Locate every malaria parasite and every leukocyte.
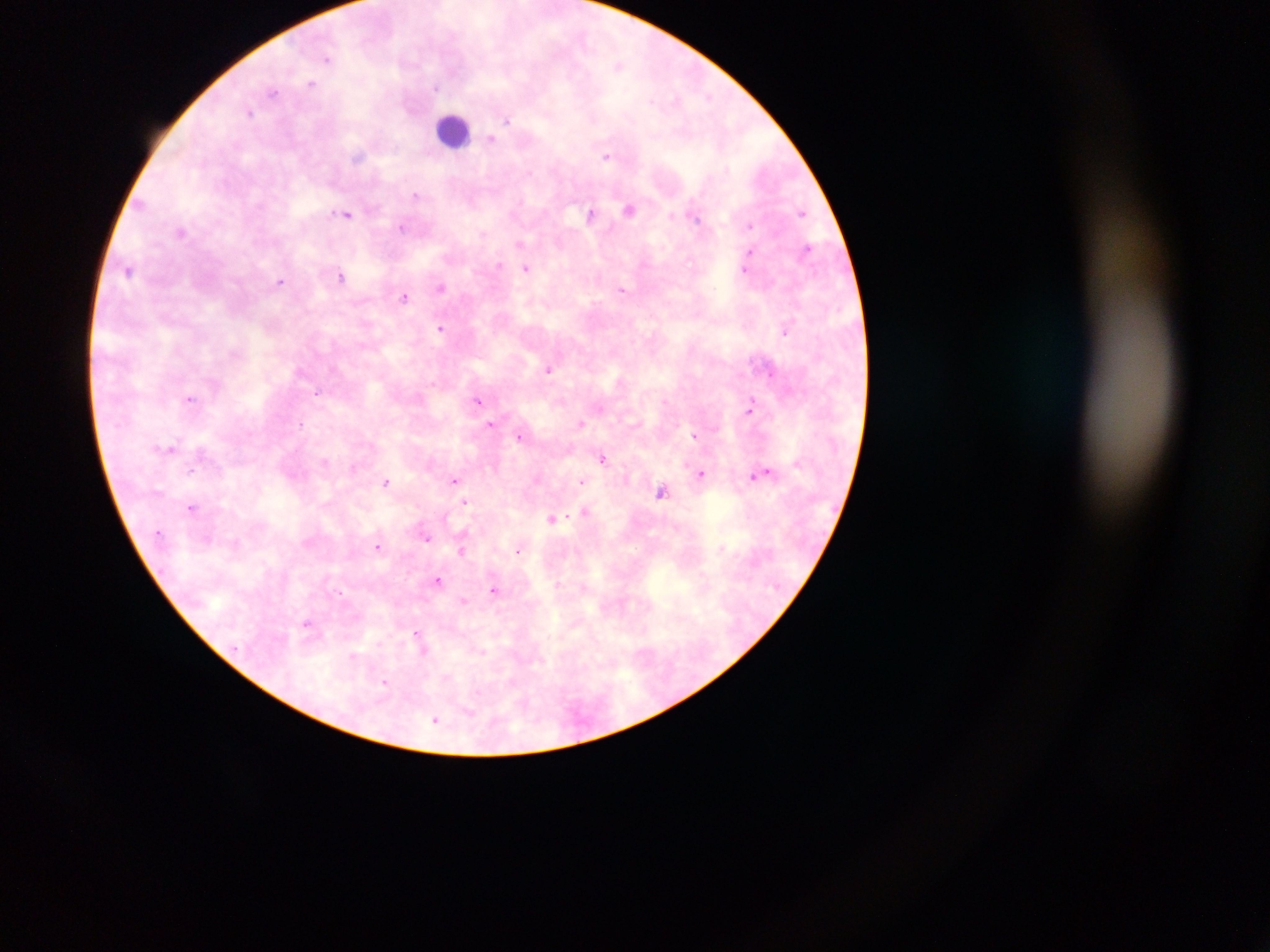

Approximate centers as {x, y} in pixels.
Malaria parasites: {327, 58}, {619, 66}, {311, 84}, {436, 87}, {273, 92}, {651, 100}, {250, 112}, {507, 120}, {491, 139}, {606, 155}, {358, 157}, {530, 173}, {415, 194}, {142, 204}, {629, 209}, {802, 212}, {347, 214}, {590, 214}, {672, 216}, {696, 217}, {748, 225}, {402, 227}, {182, 232}, {807, 249}, {750, 252}, {499, 266}, {526, 267}, {745, 269}, {129, 271}, {341, 276}, {280, 282}, {441, 288}, {621, 289}, {404, 298}, {440, 327}, {785, 331}, {548, 369}, {317, 393}, {189, 398}, {477, 402}, {750, 406}, {581, 422}, {301, 423}, {491, 425}, {694, 435}, {519, 436}, {169, 448}, {603, 458}, {324, 462}, {191, 471}, {768, 473}, {701, 474}, {753, 476}, {455, 479}, {386, 481}, {581, 481}, {661, 491}, {466, 501}, {192, 507}, {585, 512}, {552, 519}, {427, 537}, {378, 546}, {518, 550}, {461, 551}, {438, 579}, {493, 590}, {463, 601}, {306, 623}, {417, 634}, {423, 649}, {353, 656}, {385, 682}, {435, 719}.
Leukocytes: {453, 130}.

Summary:
  - Capture: mobile-phone photograph through a microscope
  - Country: Ghana
  - Field of view: single
  - Image size: 1270×952 pixels
  - Preparation: thick blood film